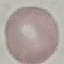
result: no malaria parasites seen
capture: smartphone through the microscope eyepiece
image_type: cell patch, automatically extracted from a larger field of view and resized to 64 × 64 pixels
preparation: thin blood film
stain: Giemsa